Point out each Plasmodium parasite.
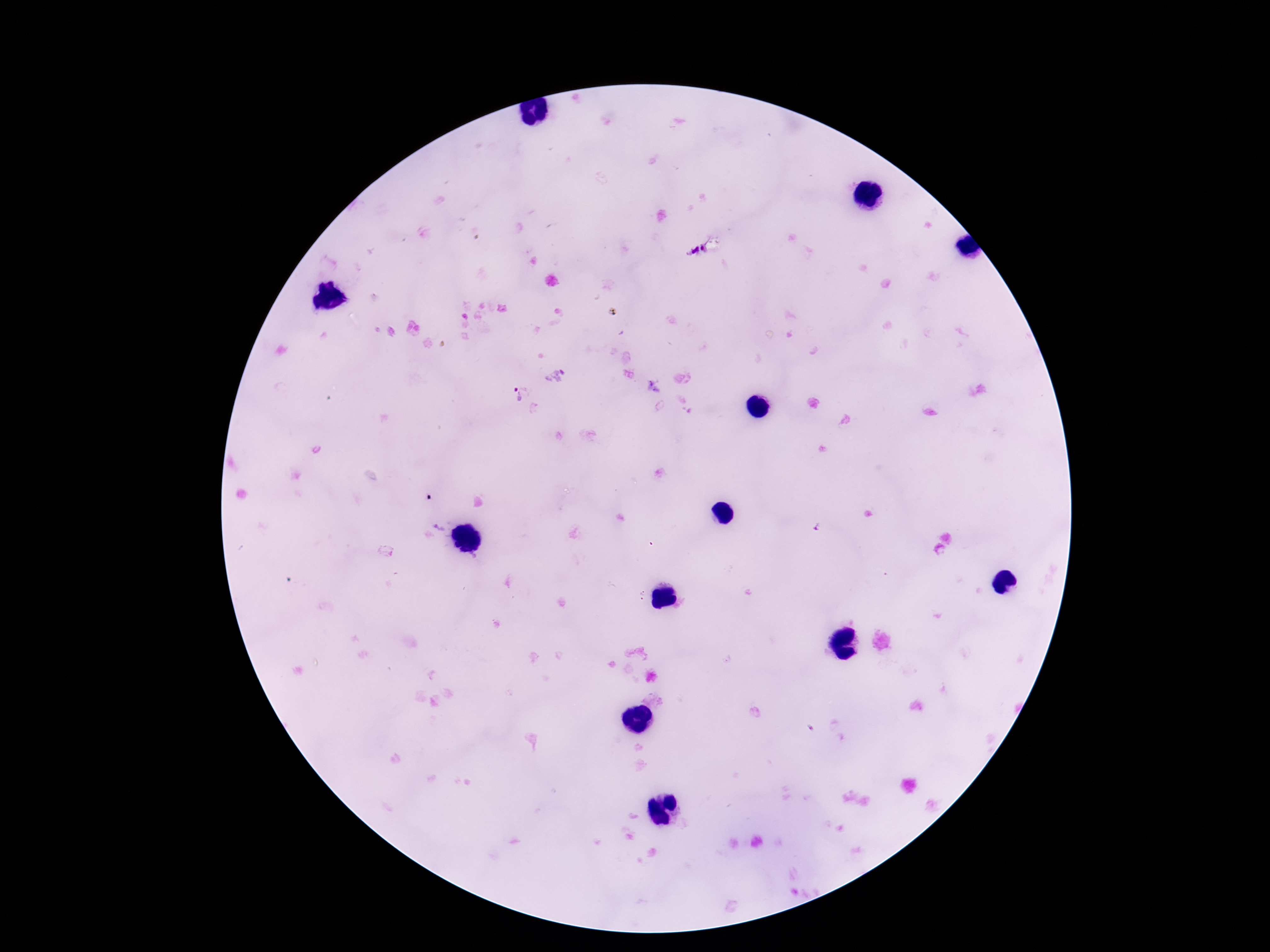

Approximate centers as {x, y} in pixels.
Plasmodium parasites: {696, 250}, {555, 375}, {517, 396}.

Summary:
  - Capture: smartphone camera through the microscope eyepiece
  - Field of view: one from this slide
  - Magnification: 100x
  - Image size: 1270×952 pixels
  - Stain: Giemsa
  - Patient malaria status: positive
  - Preparation: thick blood film